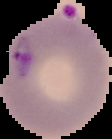
Summary:
  - Image type: segmented cell region with the area outside set to black
  - Preparation: thin blood film
  - Malaria status: parasitized
  - Image size: 112×139 pixels